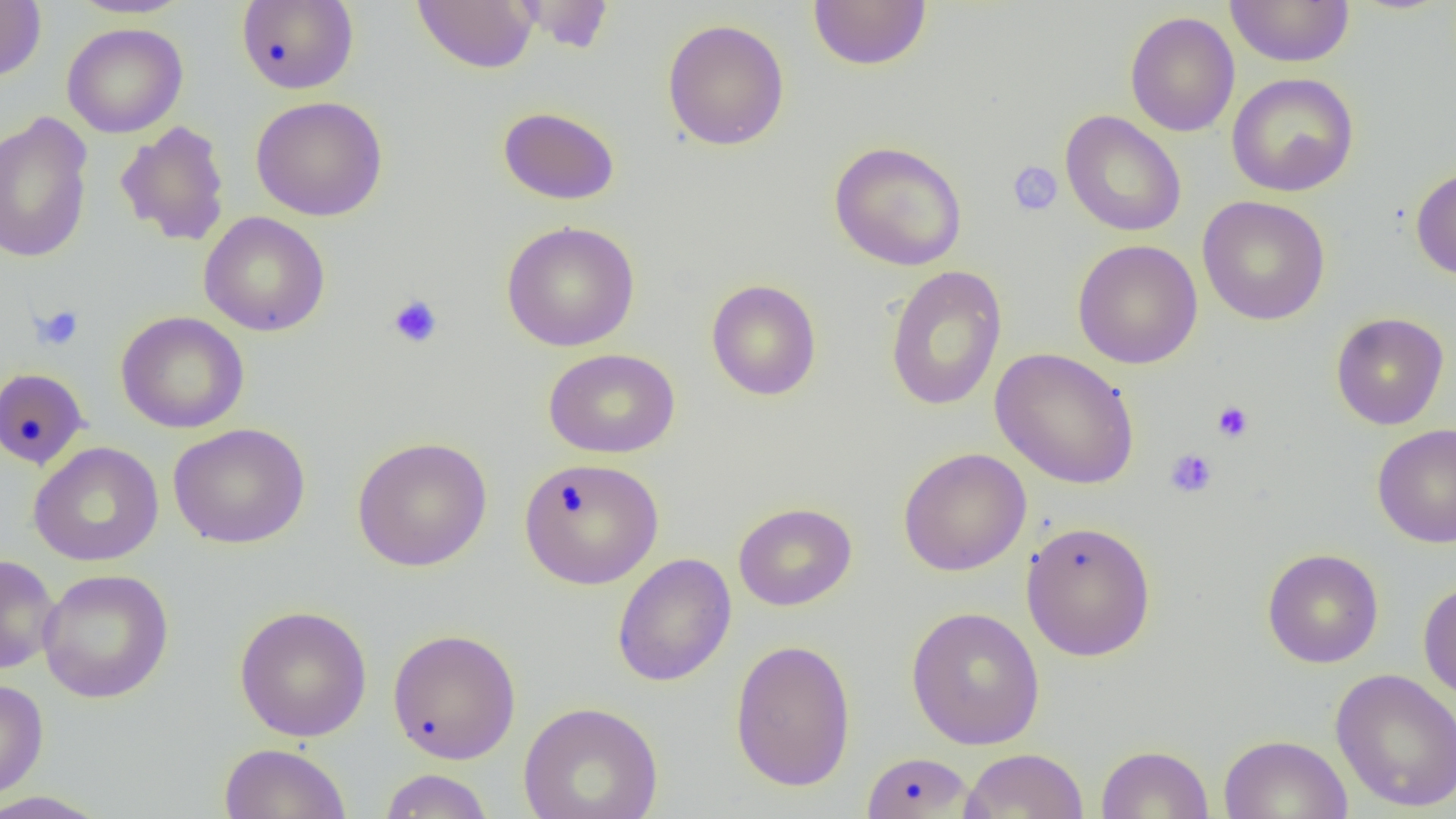

Approximate bounding boxes as named x1/y1/x2/y2 corners in pixels. Platelet locations: (x1=1007, y1=161, x2=1063, y2=216), (x1=387, y1=293, x2=443, y2=348), (x1=31, y1=305, x2=84, y2=351), (x1=1212, y1=401, x2=1254, y2=443), (x1=1165, y1=448, x2=1218, y2=498). Uninfected red blood cell locations: (x1=66, y1=0, x2=194, y2=19), (x1=413, y1=0, x2=539, y2=73), (x1=513, y1=0, x2=615, y2=54), (x1=1225, y1=0, x2=1355, y2=67), (x1=0, y1=1, x2=46, y2=82), (x1=235, y1=1, x2=359, y2=94), (x1=808, y1=1, x2=931, y2=71), (x1=1124, y1=11, x2=1240, y2=137), (x1=662, y1=18, x2=790, y2=151), (x1=62, y1=23, x2=188, y2=138), (x1=1226, y1=72, x2=1360, y2=197), (x1=250, y1=95, x2=388, y2=221), (x1=497, y1=106, x2=620, y2=205), (x1=1060, y1=110, x2=1186, y2=237), (x1=0, y1=111, x2=94, y2=264), (x1=115, y1=120, x2=231, y2=246), (x1=829, y1=140, x2=968, y2=271), (x1=1410, y1=164, x2=1456, y2=281), (x1=1197, y1=195, x2=1330, y2=326), (x1=198, y1=211, x2=331, y2=336), (x1=501, y1=221, x2=640, y2=352), (x1=1072, y1=239, x2=1203, y2=369), (x1=885, y1=265, x2=1008, y2=411), (x1=705, y1=278, x2=822, y2=401), (x1=115, y1=310, x2=249, y2=434), (x1=1331, y1=312, x2=1449, y2=430), (x1=543, y1=347, x2=681, y2=459), (x1=990, y1=348, x2=1140, y2=490), (x1=0, y1=367, x2=89, y2=470), (x1=168, y1=422, x2=310, y2=549), (x1=1372, y1=422, x2=1456, y2=548), (x1=352, y1=436, x2=492, y2=572), (x1=28, y1=441, x2=164, y2=566), (x1=897, y1=447, x2=1032, y2=576), (x1=518, y1=457, x2=664, y2=590), (x1=733, y1=502, x2=857, y2=611), (x1=1020, y1=520, x2=1157, y2=661), (x1=1262, y1=549, x2=1384, y2=668), (x1=612, y1=553, x2=737, y2=687), (x1=0, y1=554, x2=60, y2=674), (x1=37, y1=568, x2=174, y2=704), (x1=1418, y1=580, x2=1456, y2=704), (x1=233, y1=604, x2=373, y2=742), (x1=906, y1=606, x2=1046, y2=750), (x1=387, y1=628, x2=522, y2=764), (x1=730, y1=639, x2=856, y2=791), (x1=1329, y1=668, x2=1456, y2=813), (x1=0, y1=677, x2=49, y2=801), (x1=518, y1=700, x2=663, y2=819), (x1=1218, y1=733, x2=1353, y2=818), (x1=219, y1=742, x2=352, y2=819), (x1=1095, y1=744, x2=1214, y2=819), (x1=960, y1=748, x2=1089, y2=819), (x1=860, y1=751, x2=979, y2=818), (x1=378, y1=768, x2=495, y2=819), (x1=0, y1=791, x2=112, y2=819). Slide-level diagnosis: negative for blood parasites. One field of a larger specimen. Image is 1456×819 pixels. Thin blood film. 1000x magnification. Light microscopy.